Identify the cell.
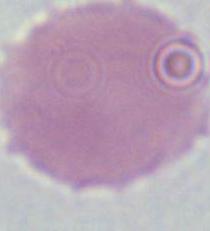

This is an erythrocyte.

Captured at 1000x magnification. Micrograph.